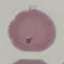

result = no malaria parasites detected
stain = Giemsa
image type = automatically extracted cell patch, resized to 64 × 64 pixels
capture = smartphone camera at the microscope eyepiece
preparation = thin blood film